Point out each leukocyte.
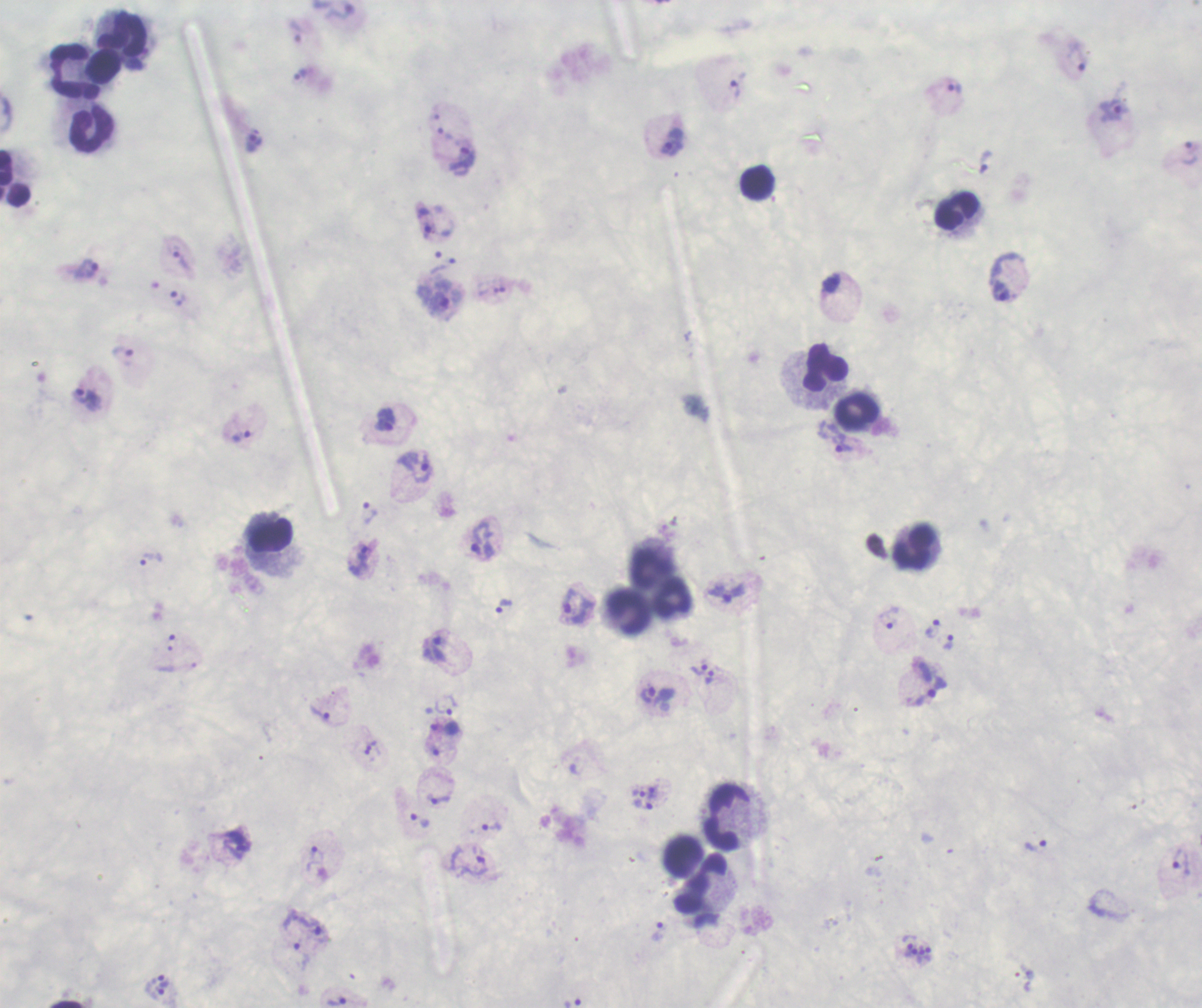

Approximate object centers, in pixels from the top-left corner.
Leukocytes: (x=125, y=39), (x=104, y=71), (x=72, y=73), (x=92, y=131), (x=15, y=179), (x=756, y=184), (x=956, y=211), (x=824, y=367), (x=856, y=415), (x=271, y=537), (x=915, y=547), (x=650, y=566), (x=672, y=598), (x=627, y=609), (x=725, y=816), (x=681, y=852), (x=701, y=886).

Approximate object centers, in pixels from the top-left corner.
Summary:
  - Trophozoite locations: (x=337, y=13), (x=296, y=32), (x=1077, y=58), (x=300, y=76), (x=953, y=88), (x=734, y=90), (x=1113, y=110), (x=670, y=140), (x=253, y=141), (x=1188, y=152), (x=463, y=159), (x=182, y=261), (x=86, y=269), (x=1002, y=291), (x=177, y=297), (x=123, y=357), (x=87, y=399), (x=385, y=419), (x=241, y=437), (x=842, y=443), (x=415, y=467), (x=368, y=512), (x=481, y=540), (x=151, y=559), (x=360, y=560), (x=503, y=607), (x=577, y=608), (x=887, y=617), (x=931, y=628), (x=948, y=642), (x=438, y=648), (x=698, y=669), (x=709, y=678), (x=928, y=692), (x=648, y=695), (x=444, y=706), (x=320, y=715), (x=646, y=794), (x=438, y=800), (x=420, y=821), (x=491, y=827), (x=1036, y=845), (x=314, y=858), (x=468, y=861), (x=1179, y=862), (x=309, y=924), (x=658, y=931), (x=300, y=956), (x=162, y=980), (x=157, y=993), (x=336, y=1002), (x=572, y=1002)
  - Magnification: 100x
  - Field of view: one from this slide
  - Background quality: unsatisfactory
  - Context: previously used in an actual diagnosis
  - Stain: Romanowsky
  - Result: positive for Plasmodium parasites
  - Preparation: thick blood smear
  - Image size: 1202×1008 pixels